Comment on the morphology of the red blood cells.
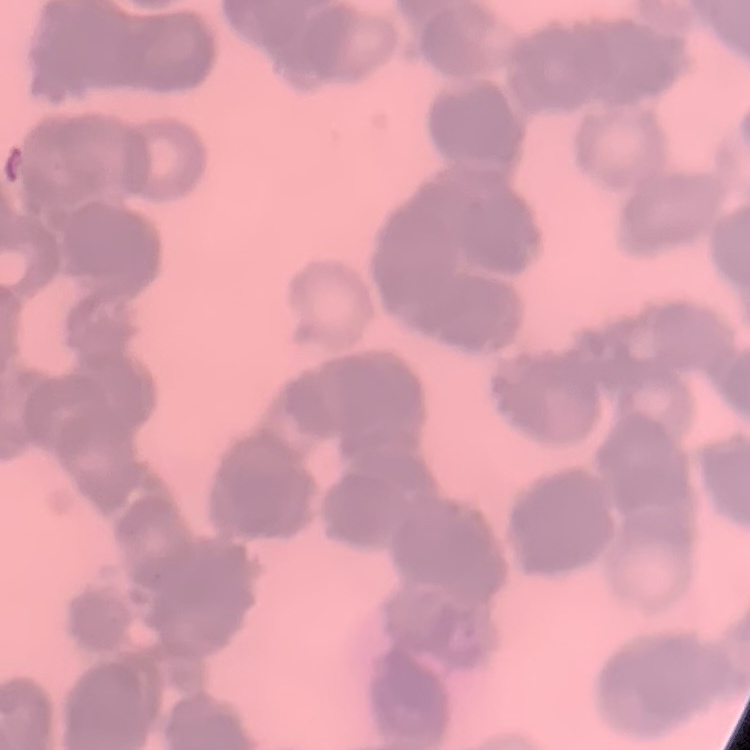
Rouleaux formation.

Summary:
  - Image type: one tile cut from a larger photomicrograph
  - Preparation: thin peripheral smear
  - Stain: Field's or Giemsa